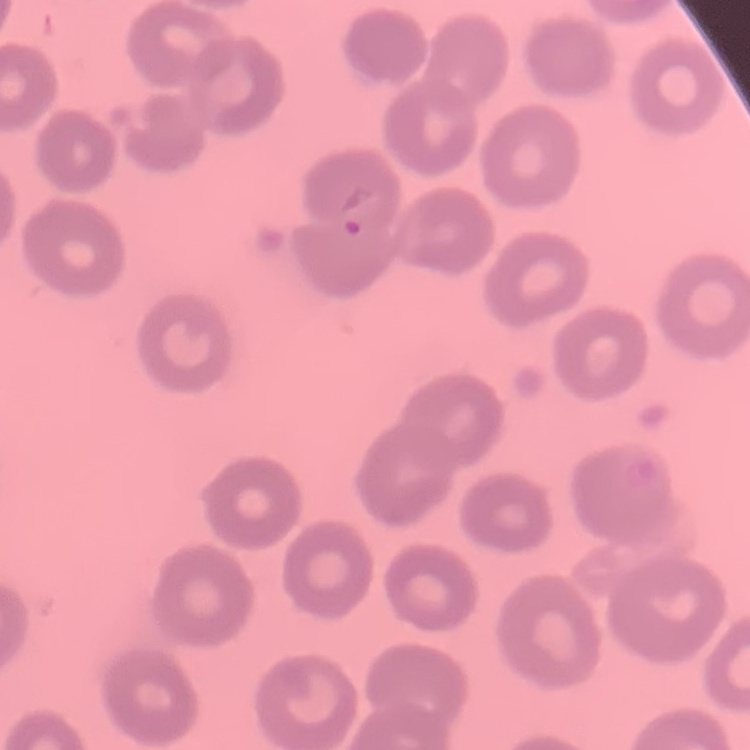

{
  "erythrocyte_morphology": "no rouleaux formation",
  "preparation": "thin peripheral smear",
  "stain": "Field's or Giemsa",
  "image_type": "one tile cut from a larger photomicrograph"
}